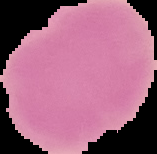
preparation = thin blood film
image size = 157×154 pixels
result = negative for malaria parasites
image type = segmented cell region on a black background